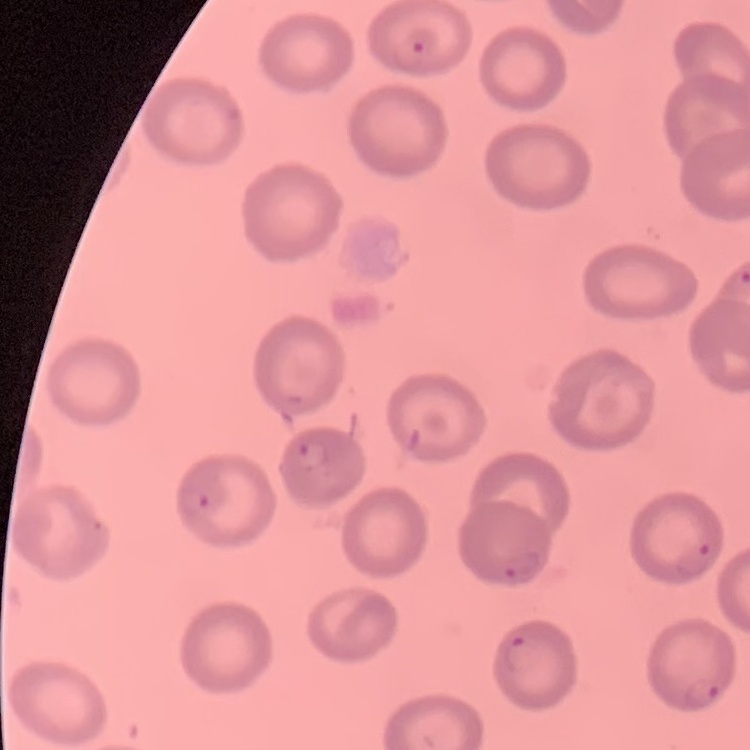
The red blood cells show no rouleaux formation. Square crop of a larger photomicrograph. Stained with either Field's or Giemsa. Thin peripheral smear.